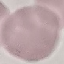
{
  "result": "no malaria parasites detected",
  "stain": "Giemsa",
  "image_type": "cell patch, automatically extracted from a larger field of view and resized to 64 × 64 pixels",
  "preparation": "thin smear",
  "capture": "smartphone camera at the microscope eyepiece"
}